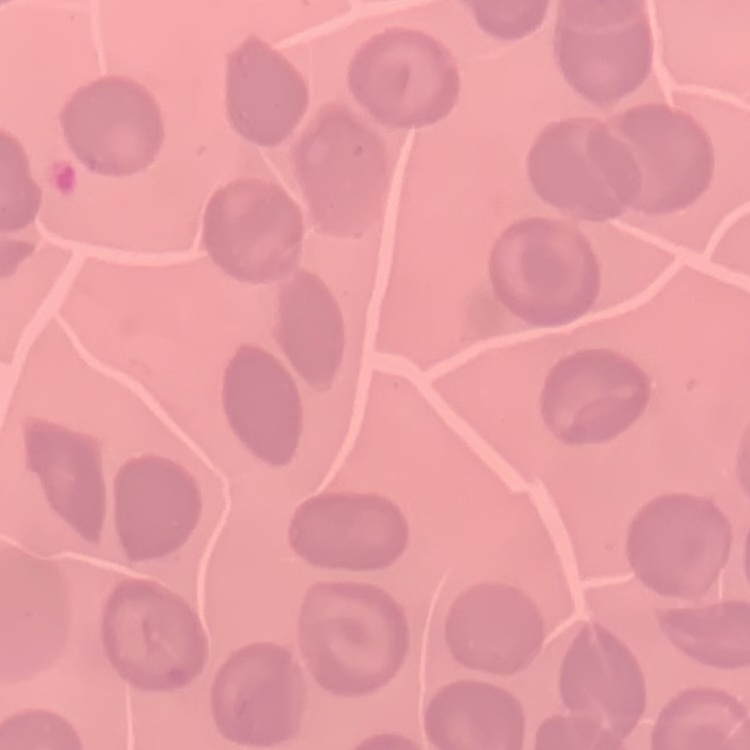
The erythrocytes exhibit no rouleaux formation. Thin blood smear. One tile cut from a larger photomicrograph. Stained with either Field's or Giemsa.